Give the extent of all Plasmodium falciparum-infected red blood cells.
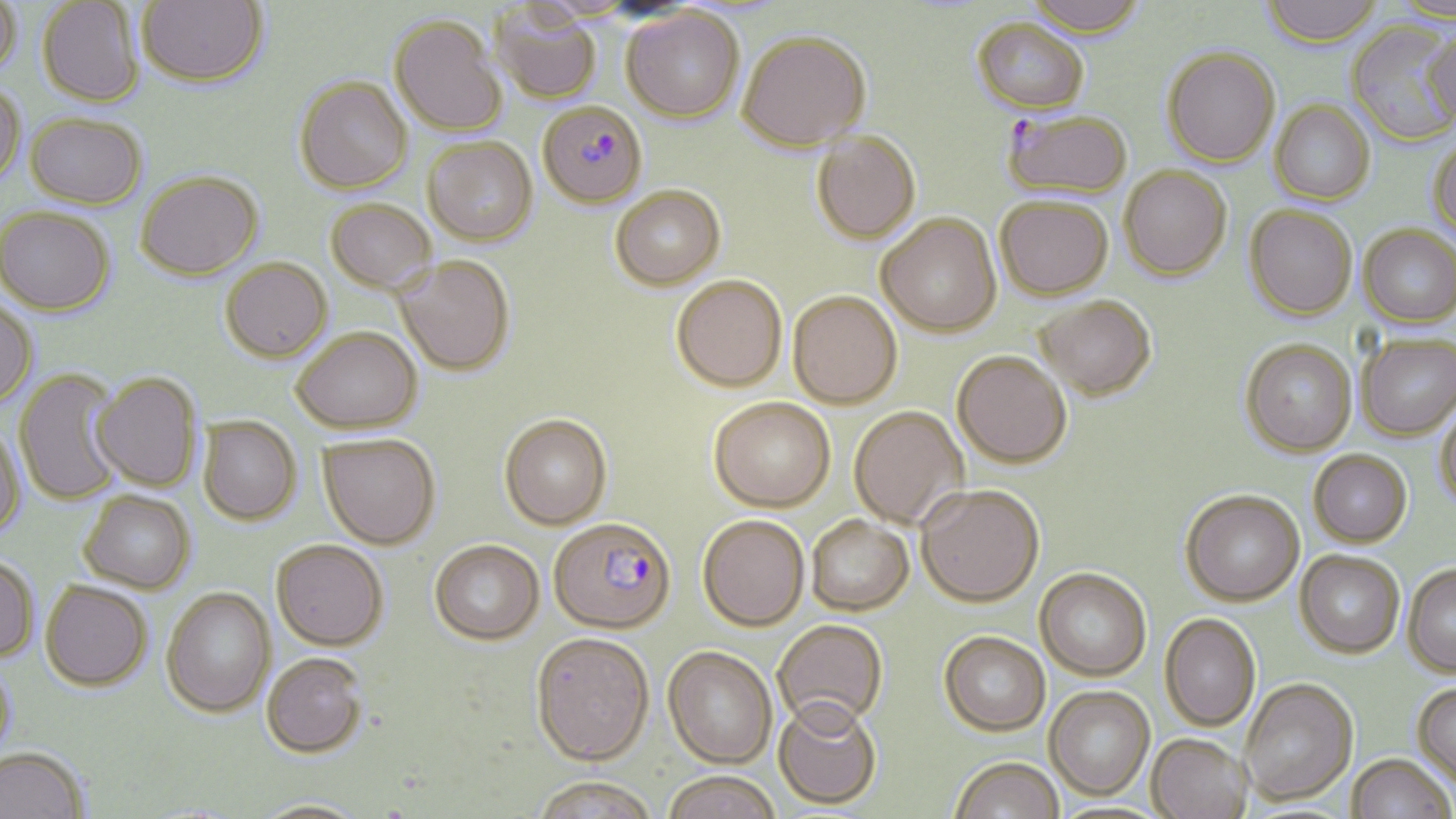

Approximate bounding boxes as named x1/y1/x2/y2 corners in pixels.
Plasmodium falciparum-infected red blood cells: (x1=532, y1=105, x2=649, y2=207), (x1=1004, y1=109, x2=1135, y2=198), (x1=548, y1=516, x2=675, y2=633).

slide-level diagnosis = Plasmodium falciparum
field of view = single
magnification = 1000x
image size = 1456×819 pixels
preparation = thin blood film
uninfected red blood cell locations = approximate bounding boxes as named x1/y1/x2/y2 corners in pixels: (x1=0, y1=0, x2=21, y2=78), (x1=136, y1=0, x2=268, y2=88), (x1=1024, y1=0, x2=1148, y2=38), (x1=1262, y1=0, x2=1384, y2=49), (x1=38, y1=1, x2=144, y2=107), (x1=1389, y1=1, x2=1456, y2=25), (x1=491, y1=5, x2=602, y2=104), (x1=621, y1=7, x2=745, y2=122), (x1=389, y1=14, x2=507, y2=136), (x1=972, y1=17, x2=1090, y2=114), (x1=1345, y1=22, x2=1456, y2=145), (x1=737, y1=29, x2=872, y2=151), (x1=1424, y1=32, x2=1456, y2=128), (x1=1162, y1=47, x2=1280, y2=167), (x1=294, y1=76, x2=413, y2=194), (x1=0, y1=81, x2=26, y2=185), (x1=1270, y1=99, x2=1375, y2=204), (x1=25, y1=112, x2=147, y2=208), (x1=811, y1=131, x2=921, y2=244), (x1=1427, y1=136, x2=1456, y2=242), (x1=422, y1=137, x2=537, y2=245), (x1=1119, y1=165, x2=1232, y2=279), (x1=136, y1=171, x2=261, y2=279), (x1=609, y1=184, x2=725, y2=289), (x1=995, y1=195, x2=1113, y2=299), (x1=325, y1=198, x2=437, y2=293), (x1=1244, y1=204, x2=1357, y2=320), (x1=0, y1=206, x2=115, y2=316), (x1=877, y1=213, x2=1001, y2=336), (x1=1359, y1=223, x2=1456, y2=327), (x1=394, y1=254, x2=514, y2=375), (x1=220, y1=257, x2=332, y2=362), (x1=671, y1=274, x2=787, y2=391), (x1=788, y1=290, x2=902, y2=408), (x1=1035, y1=295, x2=1156, y2=399), (x1=0, y1=299, x2=38, y2=407), (x1=292, y1=327, x2=423, y2=432), (x1=1357, y1=334, x2=1456, y2=439), (x1=1240, y1=338, x2=1357, y2=456), (x1=952, y1=350, x2=1071, y2=467), (x1=12, y1=370, x2=128, y2=506), (x1=91, y1=372, x2=203, y2=492), (x1=708, y1=397, x2=835, y2=511), (x1=1434, y1=397, x2=1456, y2=513), (x1=849, y1=406, x2=969, y2=529), (x1=499, y1=413, x2=611, y2=529), (x1=198, y1=416, x2=301, y2=525), (x1=0, y1=423, x2=26, y2=541), (x1=319, y1=433, x2=440, y2=549), (x1=1308, y1=449, x2=1412, y2=547), (x1=916, y1=483, x2=1044, y2=606), (x1=1180, y1=489, x2=1304, y2=605), (x1=79, y1=490, x2=196, y2=593), (x1=698, y1=514, x2=809, y2=630), (x1=806, y1=514, x2=913, y2=615), (x1=271, y1=539, x2=389, y2=650), (x1=429, y1=539, x2=544, y2=644), (x1=1295, y1=549, x2=1405, y2=657), (x1=0, y1=555, x2=40, y2=661), (x1=1402, y1=562, x2=1456, y2=676), (x1=1035, y1=567, x2=1152, y2=679), (x1=40, y1=580, x2=152, y2=691), (x1=161, y1=586, x2=275, y2=717), (x1=1160, y1=612, x2=1261, y2=731), (x1=773, y1=618, x2=887, y2=727), (x1=938, y1=630, x2=1050, y2=735), (x1=530, y1=631, x2=654, y2=764), (x1=663, y1=645, x2=777, y2=767), (x1=262, y1=652, x2=368, y2=757), (x1=0, y1=658, x2=17, y2=769), (x1=1239, y1=676, x2=1358, y2=805), (x1=1412, y1=681, x2=1456, y2=789), (x1=1044, y1=684, x2=1155, y2=799), (x1=774, y1=696, x2=882, y2=809), (x1=1147, y1=733, x2=1253, y2=819), (x1=0, y1=746, x2=89, y2=819), (x1=1347, y1=753, x2=1454, y2=818), (x1=949, y1=756, x2=1065, y2=819), (x1=661, y1=770, x2=783, y2=819), (x1=528, y1=775, x2=660, y2=819), (x1=248, y1=798, x2=372, y2=818)
modality = optical microscopy
stain = May-Grünwald-Giemsa